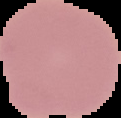

Summary:
  - Image type: cell region segmented out of the field of view; surrounding area masked to black
  - Preparation: thin blood film
  - Result: negative for Plasmodium parasites
  - Image size: 121×118 pixels